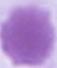
identification = red blood cell
magnification = 1000x
modality = micrograph